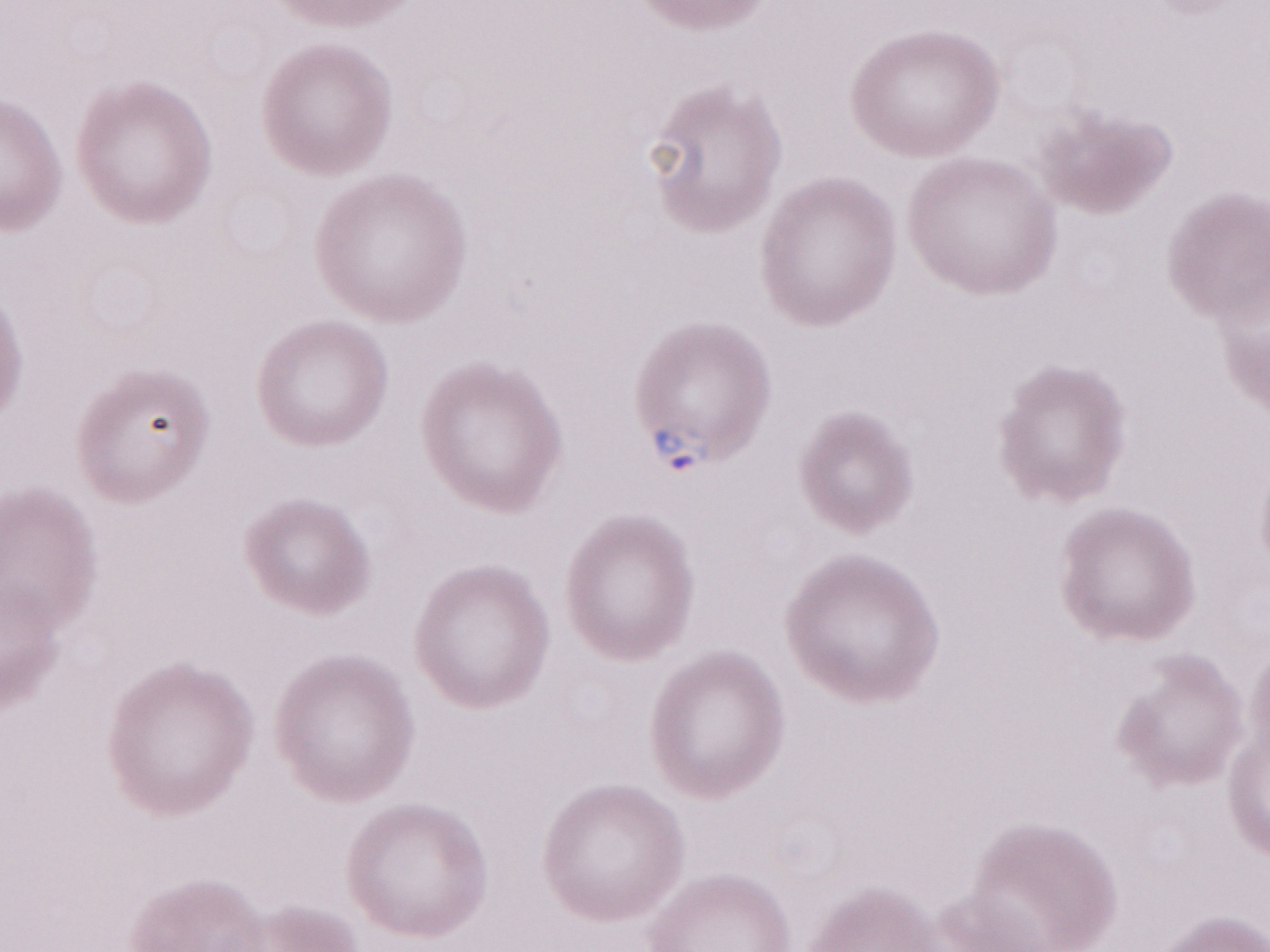

Image is 1270×952 pixels. One field of this slide. May-Grünwald-Giemsa-stained preparation. Olympus BX43 microscope, Olympus DP73 camera. 1,000x magnification. Thin peripheral-blood smear. Malaria diagnosis (patient-level): positive.